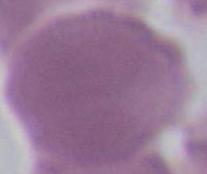
Summary:
  - Magnification: 1000x
  - Modality: micrograph
  - Identification: red blood cell